Assess the morphology of the red blood cells.
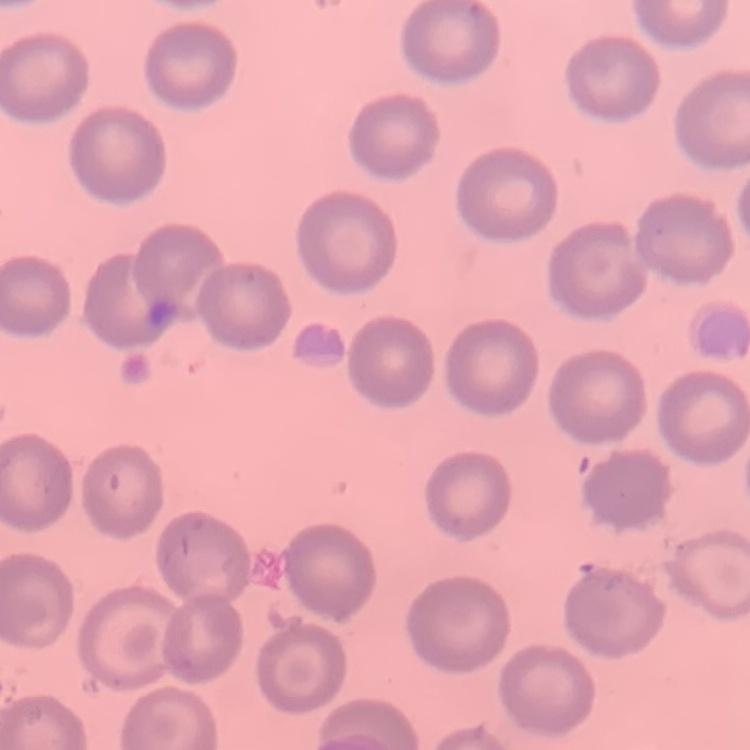

They show no rouleaux formation.

preparation = thin peripheral smear
image type = one tile cut from a larger photomicrograph
stain = Field's or Giemsa